Report the malaria status of this cell.
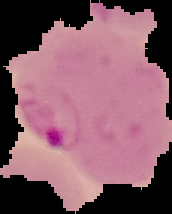

Parasitized.

preparation = thin blood smear
image size = 172×214 pixels
image type = segmented cell region on a black background